Classify this cell by malaria status.
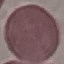
It is uninfected.

Summary:
  - Image type: automatically extracted cell patch, resized to 64 × 64 pixels
  - Capture: smartphone through the microscope eyepiece
  - Preparation: thin smear
  - Stain: Giemsa